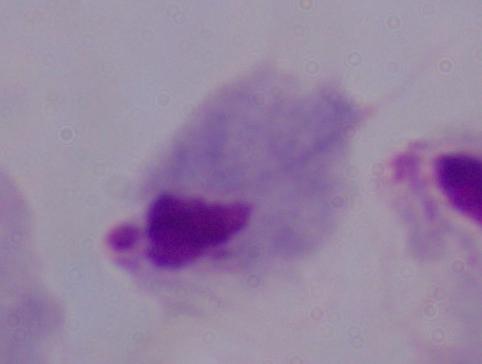

1000x magnification. Micrograph. A trichomonad is shown.